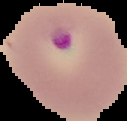

Summary:
  - Image type: segmented cell region with the area outside set to black
  - Preparation: thin blood smear
  - Result: Plasmodium parasites detected
  - Image size: 127×121 pixels